Assess this cell for malaria.
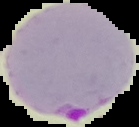

Parasitized.

Summary:
  - Image type: segmented cell region on a black background
  - Preparation: thin blood film
  - Image size: 139×127 pixels